Report the malaria status of this cell.
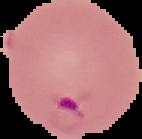
It is parasitized.

Summary:
  - Image type: segmented cell region on a black background
  - Image size: 142×139 pixels
  - Preparation: thin blood smear